Locate every malaria parasite.
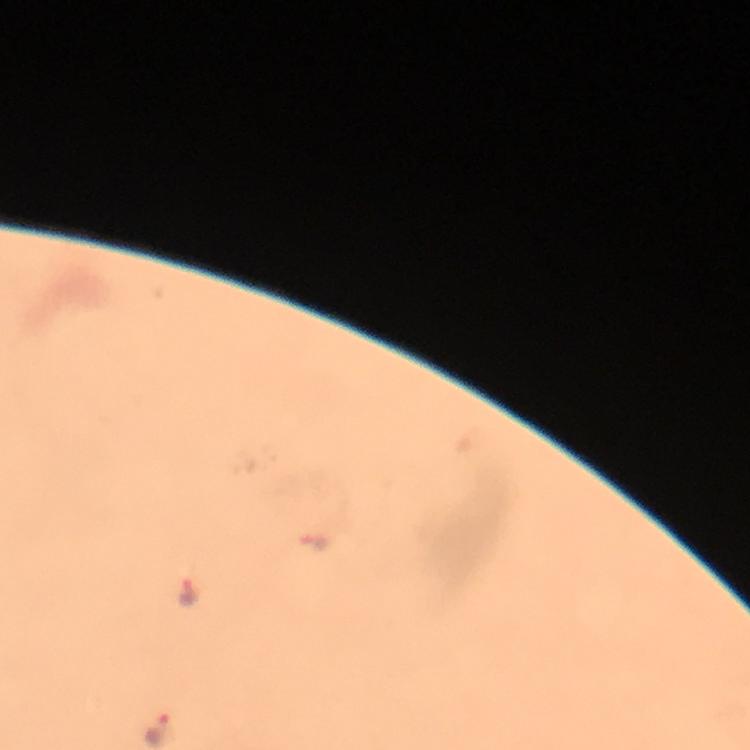
Approximate object centers, in pixels from the top-left corner.
Malaria parasites: (x=316, y=543), (x=186, y=592), (x=160, y=730).

Summary:
  - Cropped from: one field of view
  - Capture: smartphone photograph through a microscope
  - Preparation: thick blood smear
  - Context: from a diagnostic examination for malaria
  - Magnification: 100x
  - Immersion oil: used
  - Stain: Giemsa
  - Image size: 750×750 pixels